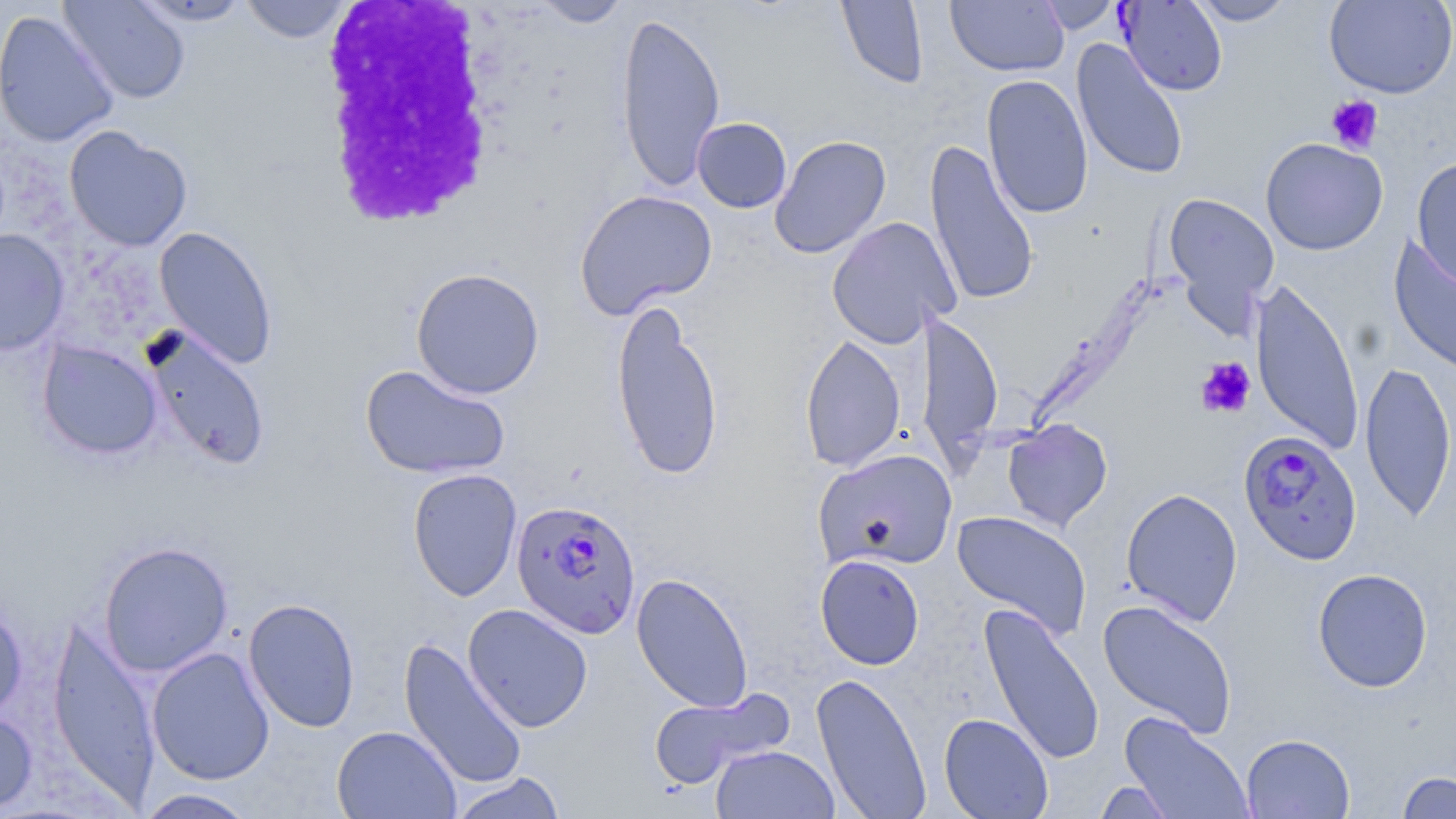 Approximate bounding boxes as (x1, y1, x2, y2) in pixels. White blood cell locations: (318, 2, 510, 229). Plasmodium falciparum-infected red blood cell locations (subset): (1239, 429, 1362, 565), (511, 499, 642, 640). Platelet locations: (1326, 95, 1384, 154), (1195, 357, 1256, 418). Uninfected red blood cell locations (subset): (58, 0, 191, 105), (131, 0, 251, 26), (239, 0, 355, 43), (531, 0, 632, 27), (836, 0, 929, 89), (1034, 0, 1123, 34), (1188, 0, 1297, 26), (1324, 0, 1456, 99), (946, 1, 1068, 76), (1, 10, 120, 148), (616, 11, 726, 193), (1072, 39, 1189, 182), (982, 74, 1094, 219), (692, 117, 792, 213), (64, 125, 193, 252), (769, 135, 891, 259), (1260, 137, 1388, 255), (924, 140, 1039, 307), (1411, 157, 1456, 292), (574, 189, 718, 319), (1163, 192, 1280, 324), (826, 216, 960, 348), (154, 226, 278, 369), (0, 229, 69, 356), (1389, 236, 1456, 380), (410, 267, 545, 398), (1249, 278, 1365, 455), (610, 299, 724, 481), (916, 309, 1004, 467), (143, 327, 271, 471), (800, 333, 906, 473), (37, 341, 163, 460), (1359, 359, 1456, 523), (360, 364, 511, 480), (1002, 419, 1113, 532), (813, 449, 957, 571), (407, 468, 522, 602), (1121, 487, 1243, 626), (952, 510, 1092, 641), (98, 541, 234, 676), (815, 554, 925, 670), (1312, 568, 1433, 692), (631, 573, 754, 713), (0, 595, 28, 722), (243, 598, 361, 733), (1097, 599, 1238, 738), (978, 603, 1105, 767), (462, 604, 593, 732), (46, 615, 162, 806), (398, 637, 528, 791), (147, 647, 275, 785), (811, 671, 932, 819), (647, 687, 794, 790), (0, 710, 38, 815), (1120, 712, 1254, 819), (939, 713, 1053, 818), (332, 725, 461, 819), (1241, 733, 1354, 818), (711, 745, 840, 819), (447, 771, 567, 819), (1395, 771, 1456, 818), (1093, 780, 1178, 818), (131, 788, 261, 818). Slide-level diagnosis: Plasmodium falciparum. Optical microscopy. Captured at 1000x magnification. One field of a larger specimen. Image is 1456×819 pixels. Thin blood smear. May-Grünwald-Giemsa-stained preparation.